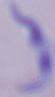

Photomicrograph. 1000x magnification. A trypanosome is seen.